Locate leukocytes (white blood cells).
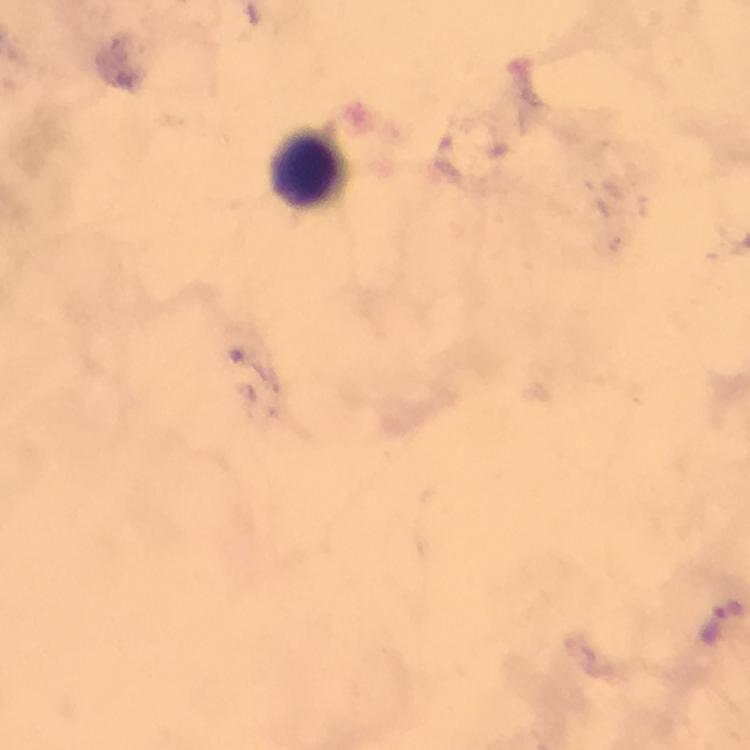
Approximate centers as [x, y] in pixels.
Leukocytes: [308, 171].

cropped from = one field of view
context = from a diagnostic examination for malaria
magnification = 100x
Plasmodium parasite locations = approximate centers as [x, y] in pixels: [726, 608]
preparation = thick blood film
capture = smartphone camera through the microscope
image size = 750×750 pixels
immersion oil = used
stain = Giemsa